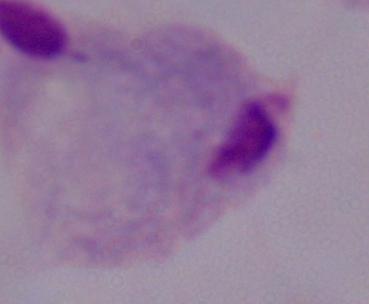
Summary:
  - Modality: micrograph
  - Identification: trichomonad
  - Magnification: 1000x